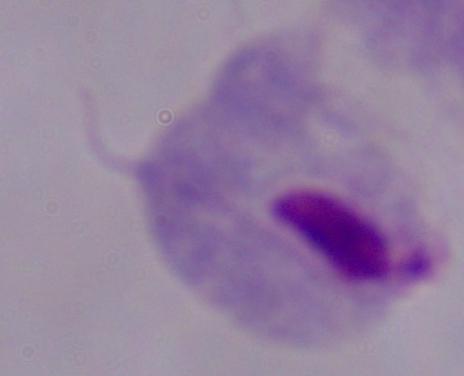

modality = photomicrograph
identification = trichomonad
magnification = 1000x